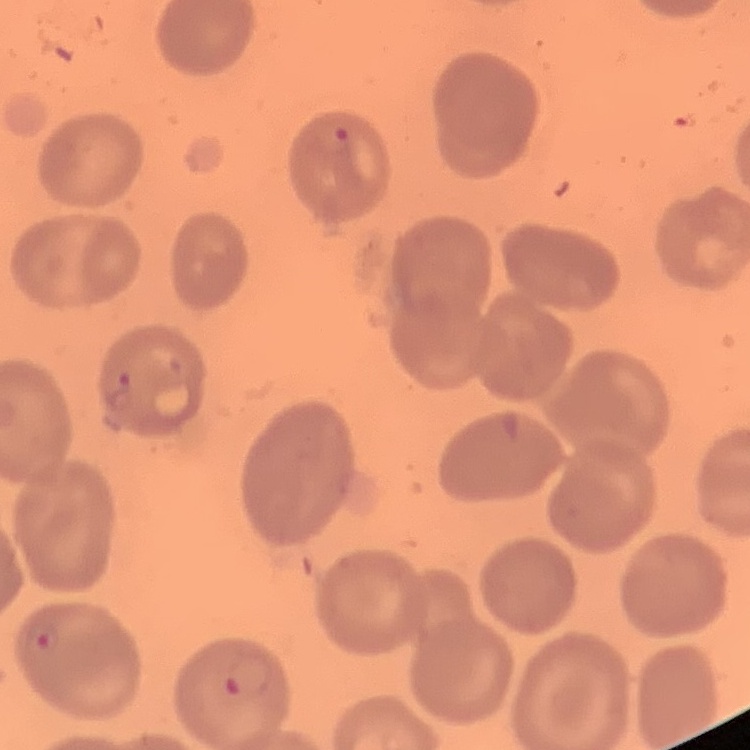

Summary:
  - Erythrocyte morphology: no rouleaux formation
  - Image type: one tile cut from a larger photomicrograph
  - Stain: Field's or Giemsa
  - Preparation: thin blood smear